Point out each Plasmodium parasite.
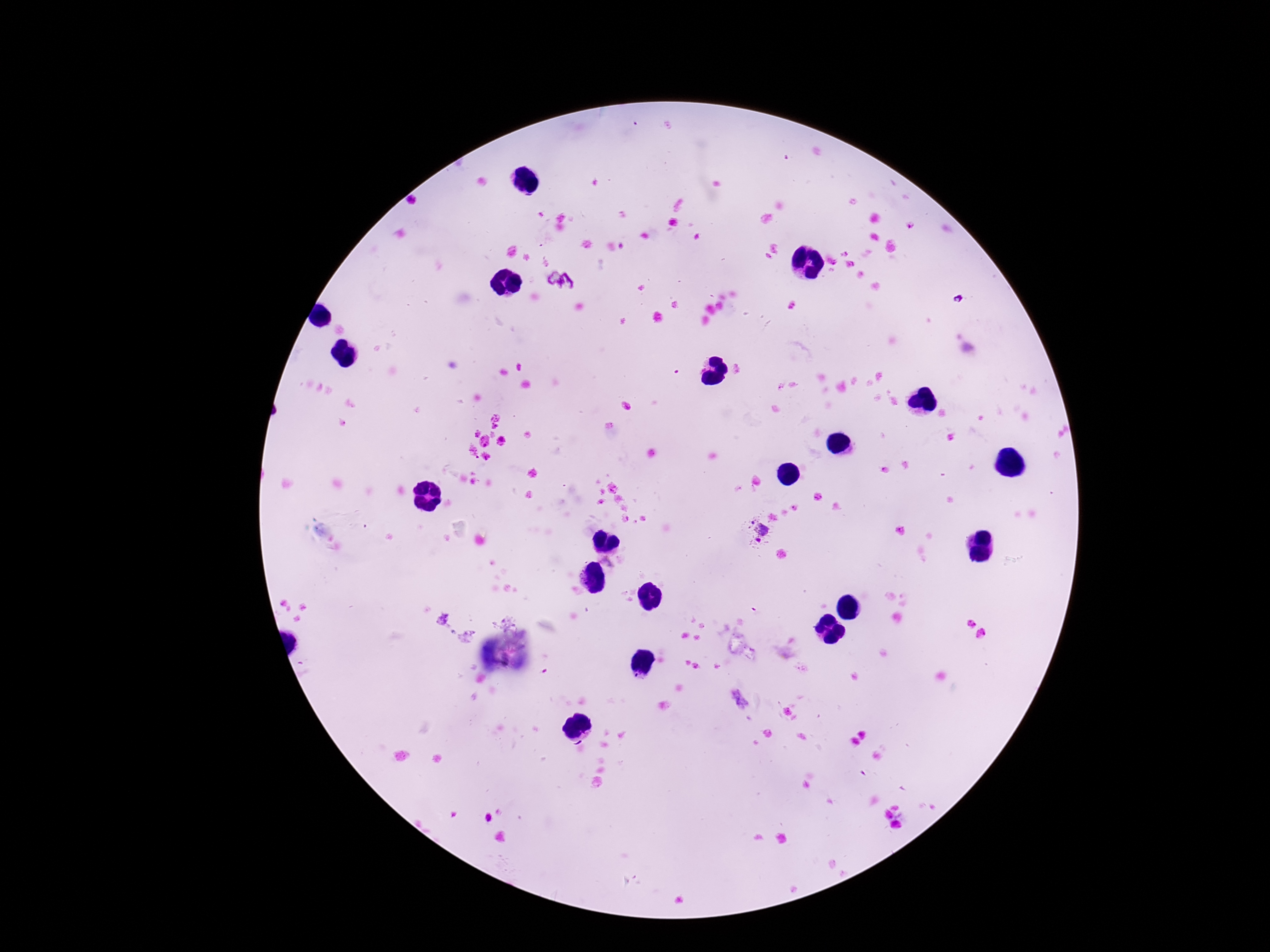
Approximate centers as [x, y] in pixels.
Plasmodium parasites: [561, 281], [958, 298], [757, 530], [442, 619], [503, 620], [466, 636], [739, 700].

One field from this slide. Thick blood smear. Giemsa-stained preparation. Image is 1270×952 pixels. Patient malaria status: infected. 100x magnification. Photographed through the microscope eyepiece with a smartphone camera.